Give the extent of all uninfected red blood cells.
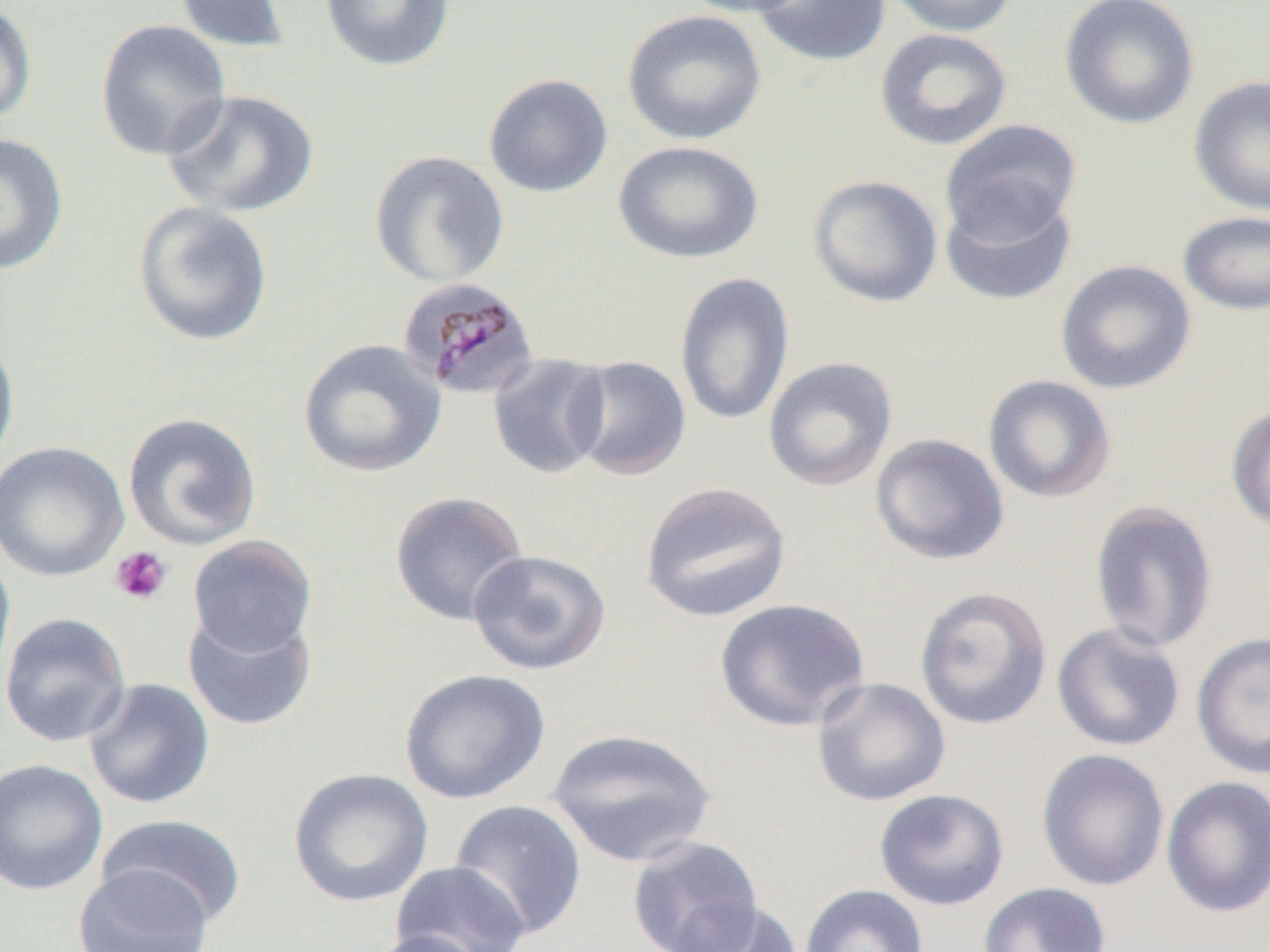
Approximate bounding boxes as [x1, y1, x2, y2] in pixels.
Uninfected red blood cells: [174, 0, 291, 53], [320, 0, 456, 72], [677, 0, 811, 18], [751, 0, 891, 68], [884, 0, 1019, 37], [1058, 0, 1200, 131], [0, 1, 38, 126], [622, 10, 766, 145], [94, 19, 231, 161], [874, 28, 1012, 151], [483, 73, 613, 198], [1188, 74, 1270, 216], [161, 90, 320, 218], [940, 120, 1081, 242], [0, 133, 68, 276], [612, 140, 764, 264], [369, 150, 509, 288], [808, 174, 943, 308], [940, 185, 1078, 307], [132, 201, 274, 347], [1177, 210, 1270, 316], [1055, 259, 1196, 395], [674, 272, 795, 428], [0, 333, 20, 476], [297, 338, 447, 478], [487, 353, 612, 479], [566, 355, 692, 481], [762, 356, 897, 492], [983, 374, 1116, 504], [1226, 404, 1270, 536], [123, 412, 262, 551], [870, 433, 1009, 566], [0, 441, 130, 582], [638, 480, 793, 623], [389, 490, 530, 627], [1090, 499, 1218, 654], [187, 534, 318, 657], [0, 547, 16, 700], [467, 548, 612, 676], [914, 585, 1052, 730], [713, 597, 871, 731], [182, 608, 317, 732], [0, 611, 133, 747], [1051, 622, 1186, 752], [1191, 631, 1270, 779], [398, 668, 551, 805], [811, 676, 951, 806], [83, 678, 216, 810], [546, 727, 717, 867], [1036, 748, 1170, 891], [0, 758, 108, 896], [288, 767, 434, 907], [1161, 775, 1270, 918], [874, 789, 1009, 910], [449, 799, 588, 940], [96, 813, 249, 927], [627, 836, 764, 952], [390, 861, 531, 952], [72, 863, 214, 952], [978, 882, 1112, 952], [798, 884, 929, 952], [670, 899, 803, 952], [363, 929, 488, 952].

Summary:
  - Plasmodium malariae-infected red blood cell locations: [396, 276, 540, 402]
  - Platelet locations: [110, 546, 173, 606]
  - Slide-level diagnosis: Plasmodium malariae
  - Preparation: thin blood film
  - Magnification: 1000x
  - Field of view: one of a larger specimen
  - Image size: 1270×952 pixels
  - Modality: optical microscopy